Assess this cell for malaria.
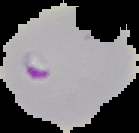

It is parasitized.

{
  "image_type": "segmented cell region on a black background",
  "image_size": "139×133 pixels",
  "preparation": "thin blood film"
}